Give the extent of all uninfected red blood cells.
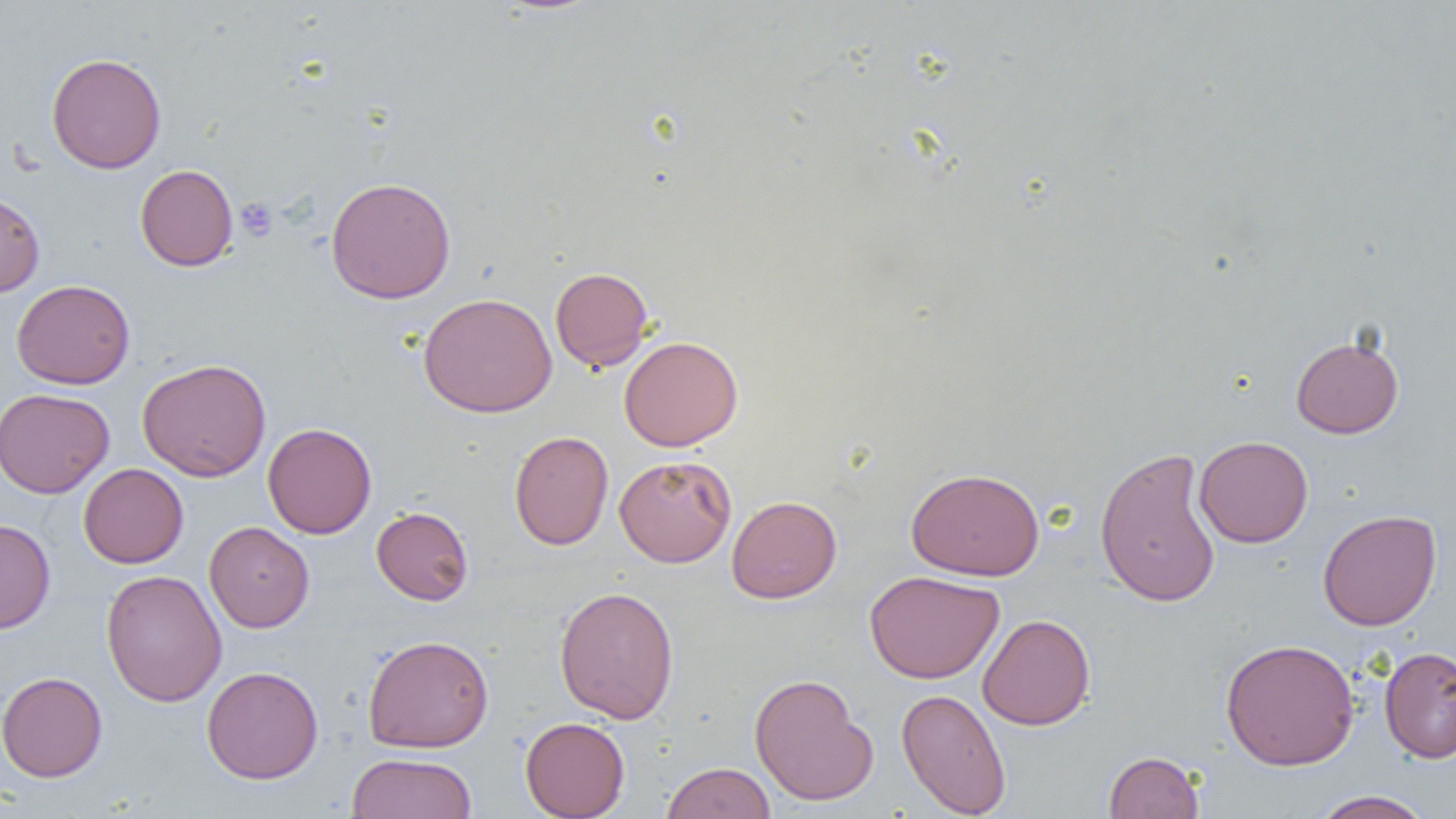

Approximate bounding boxes as named x1/y1/x2/y2 corners in pixels.
Uninfected red blood cells: (x1=46, y1=53, x2=166, y2=173), (x1=135, y1=165, x2=238, y2=271), (x1=326, y1=176, x2=456, y2=304), (x1=0, y1=191, x2=45, y2=297), (x1=550, y1=267, x2=653, y2=371), (x1=11, y1=279, x2=135, y2=389), (x1=418, y1=292, x2=557, y2=417), (x1=1290, y1=335, x2=1404, y2=438), (x1=618, y1=336, x2=743, y2=451), (x1=137, y1=358, x2=272, y2=481), (x1=0, y1=388, x2=114, y2=498), (x1=263, y1=423, x2=377, y2=539), (x1=509, y1=430, x2=613, y2=550), (x1=1194, y1=435, x2=1313, y2=548), (x1=1094, y1=445, x2=1222, y2=608), (x1=614, y1=454, x2=737, y2=567), (x1=78, y1=463, x2=188, y2=568), (x1=906, y1=467, x2=1044, y2=581), (x1=726, y1=495, x2=842, y2=603), (x1=371, y1=506, x2=473, y2=605), (x1=1317, y1=509, x2=1442, y2=630), (x1=0, y1=518, x2=55, y2=634), (x1=204, y1=521, x2=314, y2=632), (x1=101, y1=569, x2=227, y2=707), (x1=864, y1=570, x2=1004, y2=683), (x1=554, y1=585, x2=679, y2=724), (x1=977, y1=614, x2=1095, y2=730), (x1=362, y1=634, x2=494, y2=753), (x1=1220, y1=638, x2=1360, y2=770), (x1=1379, y1=646, x2=1456, y2=763), (x1=201, y1=665, x2=323, y2=784), (x1=0, y1=671, x2=107, y2=782), (x1=749, y1=673, x2=878, y2=806), (x1=896, y1=687, x2=1012, y2=818), (x1=520, y1=716, x2=630, y2=818), (x1=1103, y1=750, x2=1204, y2=819), (x1=348, y1=752, x2=477, y2=819), (x1=661, y1=761, x2=775, y2=819), (x1=1311, y1=790, x2=1433, y2=819).

Platelet locations: (x1=236, y1=197, x2=278, y2=241). Slide-level diagnosis: no evidence of blood parasites. One field of a larger specimen. Image is 1456×819 pixels. Captured at 1000x magnification. Thin blood film. Light microscopy.